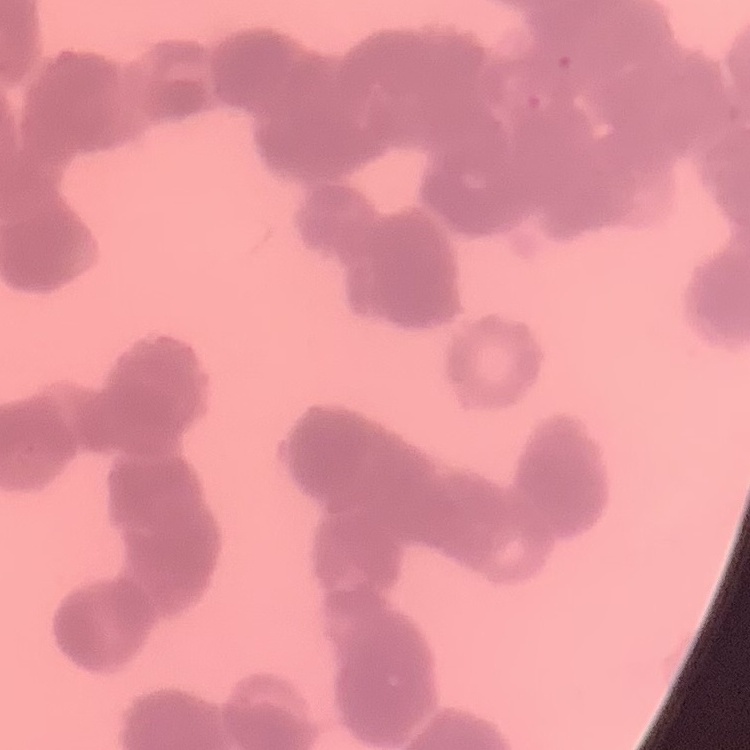

erythrocyte morphology = rouleaux formation
stain = Field's or Giemsa
image type = one tile cut from a larger photomicrograph
preparation = thin blood smear